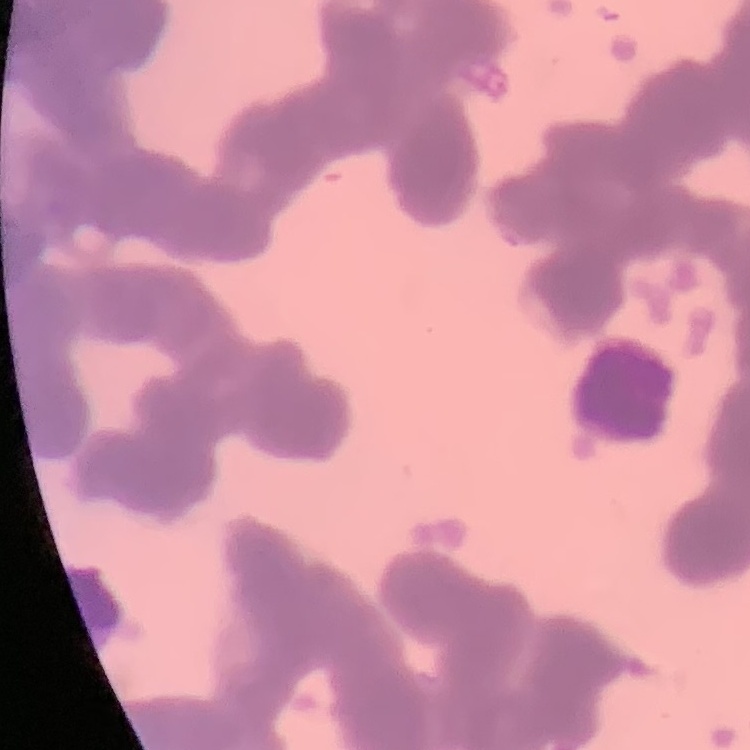

The red blood cells exhibit rouleaux formation. Thin blood film. One tile cut from a larger photomicrograph. Stained with either Field's or Giemsa.